Find the cells and give the type of each one.
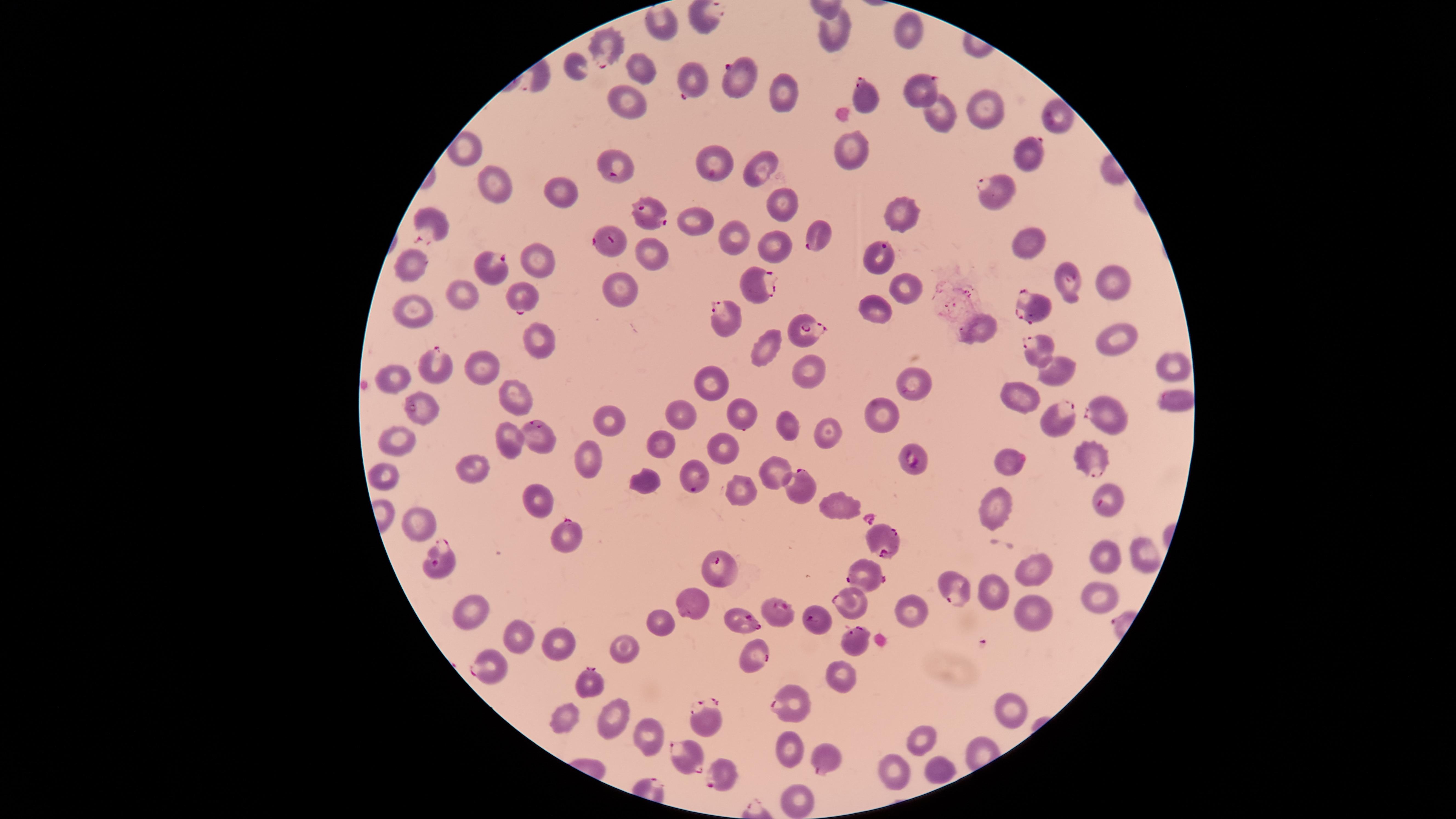

Approximate marker points as (x, y) in pixels.
Parasitized red blood cells: (703, 17), (602, 45), (737, 78), (687, 82), (919, 91), (869, 98), (1058, 117), (1030, 151), (715, 161), (617, 165), (994, 191), (651, 215), (432, 221), (818, 231), (609, 241), (879, 256), (498, 267), (1070, 278), (755, 280), (519, 295), (1036, 308), (728, 318), (805, 329), (1039, 347), (436, 361), (1179, 398), (417, 405), (1102, 411), (1062, 415), (533, 434), (1089, 455), (914, 460), (1011, 460), (691, 478), (802, 487), (1109, 502), (565, 532), (881, 539), (442, 562), (723, 566), (868, 574), (955, 591), (851, 602), (776, 611), (818, 620), (744, 621), (855, 638), (754, 654), (487, 665), (590, 681), (786, 703), (706, 722), (688, 755), (822, 758), (718, 773).
Uninfected red blood cells: (658, 22), (908, 28), (835, 32), (572, 69), (640, 70), (783, 92), (629, 101), (985, 110), (942, 118), (465, 147), (852, 147), (758, 167), (496, 183), (559, 188), (775, 207), (900, 212), (697, 221), (736, 233), (1029, 241), (774, 246), (646, 252), (542, 257), (410, 263), (1114, 281), (907, 286), (624, 287), (464, 294), (879, 303), (410, 311), (982, 325), (540, 337), (1118, 340), (766, 342), (1169, 361), (481, 364), (809, 365), (1057, 367), (907, 375), (393, 376), (713, 381), (509, 389), (1023, 400), (739, 410), (682, 412), (879, 412), (611, 420), (791, 423), (827, 424), (506, 435), (397, 439), (661, 443), (727, 448), (584, 453), (476, 464), (773, 469), (385, 472), (645, 480), (744, 489), (535, 497), (841, 507), (998, 508), (420, 522), (1144, 552), (1101, 557), (1035, 575), (998, 588), (1101, 592), (700, 601), (465, 608), (912, 609), (1035, 615), (663, 623), (519, 637), (562, 649), (623, 650), (842, 667), (1011, 710), (613, 716), (563, 717), (925, 735), (644, 736), (792, 745), (932, 765), (899, 769), (797, 794).
No white blood cells identified.

Photographed with a smartphone camera through the microscope eyepiece. Species: Plasmodium falciparum. Image is 1456×819 pixels. Thin blood film. Circular visible region. Single field of view. Giemsa stain.